Report the malaria status of this cell.
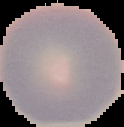

It is uninfected.

image size = 124×127 pixels
preparation = thin blood film
image type = cell region segmented out of the field of view; surrounding area masked to black